Assess the morphology of the erythrocytes.
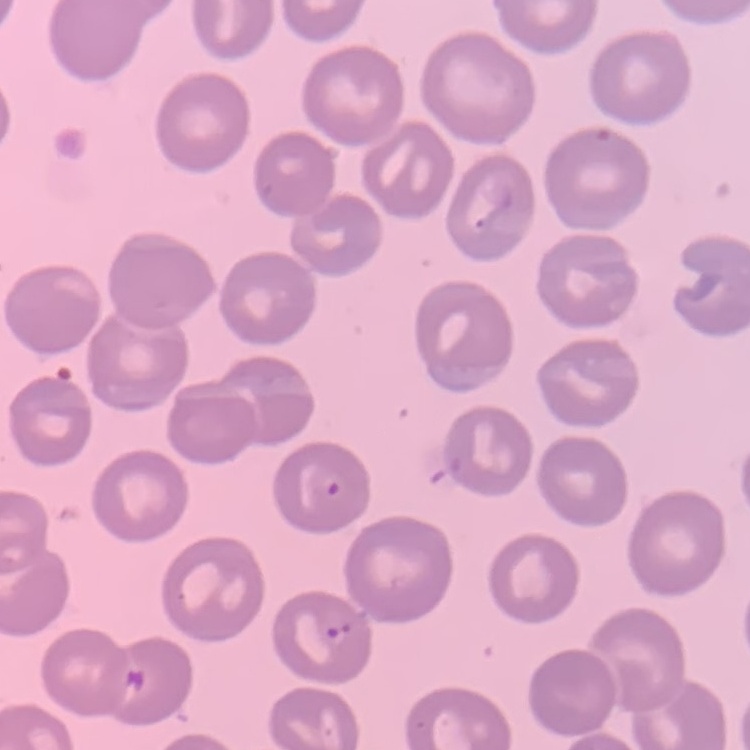

They show no rouleaux formation.

One tile cut from a larger photomicrograph. Stained with either Field's or Giemsa. Thin peripheral smear.